Assess this cell for malaria.
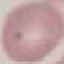

Uninfected.

Giemsa stain. Acquired by smartphone through the microscope eyepiece. Cell patch, automatically extracted from a larger field of view and resized to 64 × 64 pixels. Thin blood smear.